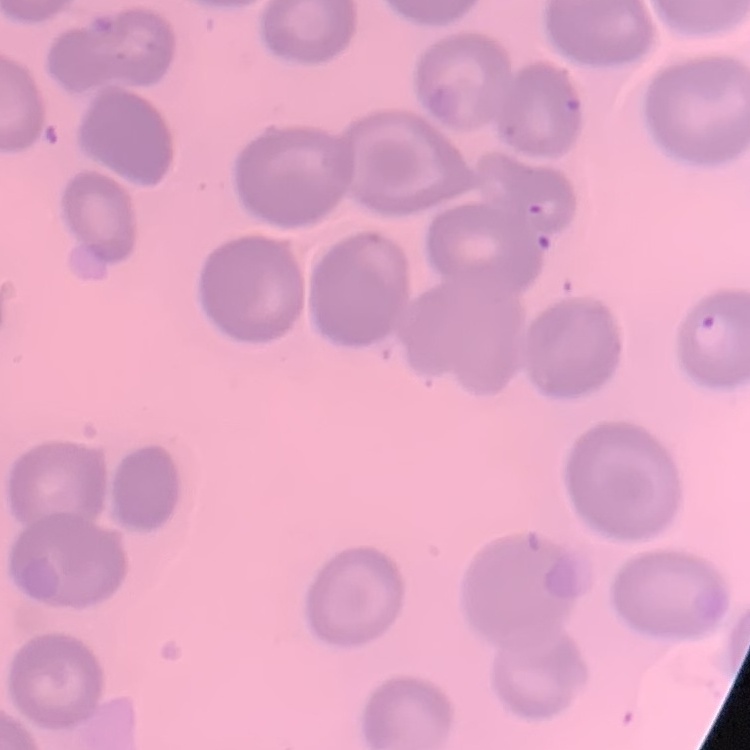
The erythrocytes show no rouleaux formation. One tile cut from a larger photomicrograph. Field's or Giemsa stain. Thin blood smear.